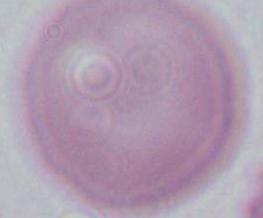
Summary:
  - Modality: photomicrograph
  - Magnification: 1000x
  - Identification: red blood cell